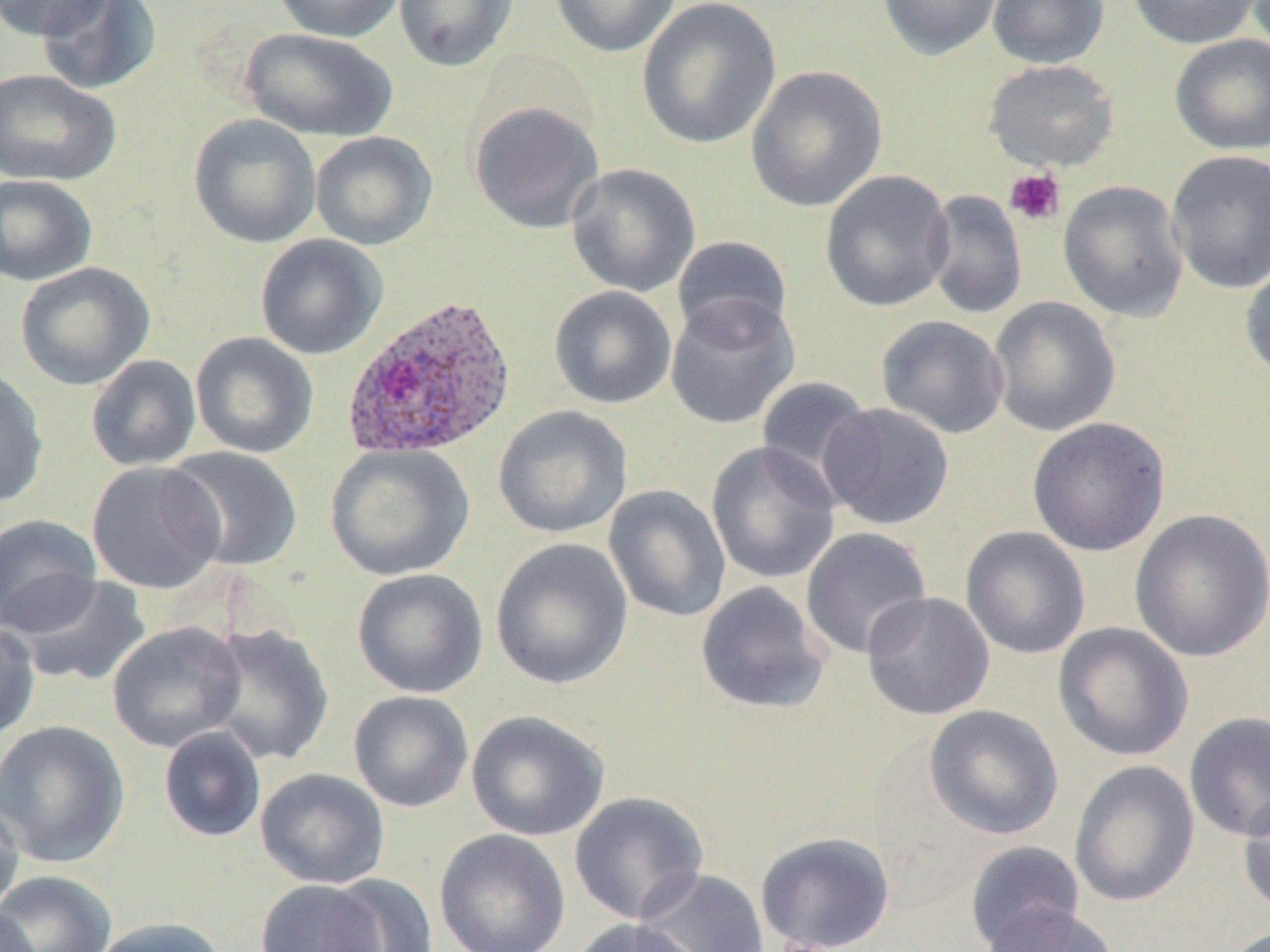

Summary:
  - Coordinate format: approximate bounding boxes as (x1, y1, x2, y2) in pixels
  - Platelet locations: (1004, 168, 1066, 226)
  - Plasmodium ovale-infected red blood cell locations: (340, 293, 518, 461)
  - Uninfected red blood cell locations: (0, 0, 111, 41), (35, 0, 163, 96), (272, 0, 406, 43), (393, 0, 519, 73), (549, 0, 681, 58), (637, 0, 781, 150), (877, 0, 1004, 60), (986, 0, 1110, 68), (1126, 0, 1264, 50), (240, 27, 398, 142), (1169, 33, 1270, 155), (983, 59, 1120, 172), (745, 65, 887, 212), (0, 68, 121, 187), (467, 100, 605, 234), (188, 113, 322, 249), (310, 131, 438, 251), (1166, 150, 1270, 294), (565, 162, 701, 297), (820, 170, 954, 313), (0, 174, 99, 287), (1058, 180, 1189, 322), (923, 189, 1028, 320), (254, 233, 388, 361), (671, 235, 794, 344), (1240, 260, 1270, 384), (15, 262, 155, 390), (548, 285, 677, 410), (665, 292, 799, 430), (988, 296, 1121, 437), (876, 315, 1009, 439), (190, 331, 319, 459), (85, 354, 202, 472), (0, 365, 50, 509), (756, 376, 879, 495), (818, 402, 955, 531), (492, 405, 633, 539), (1027, 417, 1170, 557), (706, 441, 840, 584), (325, 443, 475, 581), (163, 446, 304, 572), (86, 460, 226, 595), (604, 484, 732, 623), (1129, 509, 1270, 662), (0, 513, 103, 636), (960, 526, 1091, 660), (800, 527, 932, 660), (490, 538, 633, 690), (351, 568, 489, 698), (8, 574, 153, 688), (695, 581, 831, 714), (862, 591, 995, 721), (0, 618, 40, 744), (107, 621, 247, 753), (201, 621, 335, 766), (1052, 622, 1194, 762), (348, 690, 474, 813), (924, 704, 1064, 839), (466, 710, 610, 841), (1184, 712, 1270, 843), (0, 719, 132, 868), (157, 726, 267, 843), (1069, 760, 1200, 908), (255, 767, 390, 889), (569, 791, 710, 925), (1238, 791, 1270, 917), (0, 794, 25, 919), (434, 829, 571, 952), (755, 831, 896, 952), (963, 841, 1086, 951), (636, 868, 770, 952), (0, 869, 118, 952), (321, 873, 440, 952), (255, 880, 386, 952), (0, 903, 40, 952), (979, 903, 1122, 952), (88, 917, 230, 952), (567, 918, 707, 952)
  - Slide-level diagnosis: Plasmodium ovale
  - Field of view: single
  - Image size: 1270×952 pixels
  - Preparation: thin blood smear
  - Magnification: 1000x
  - Stain: May-Grünwald-Giemsa
  - Modality: light microscopy